Outline platelets.
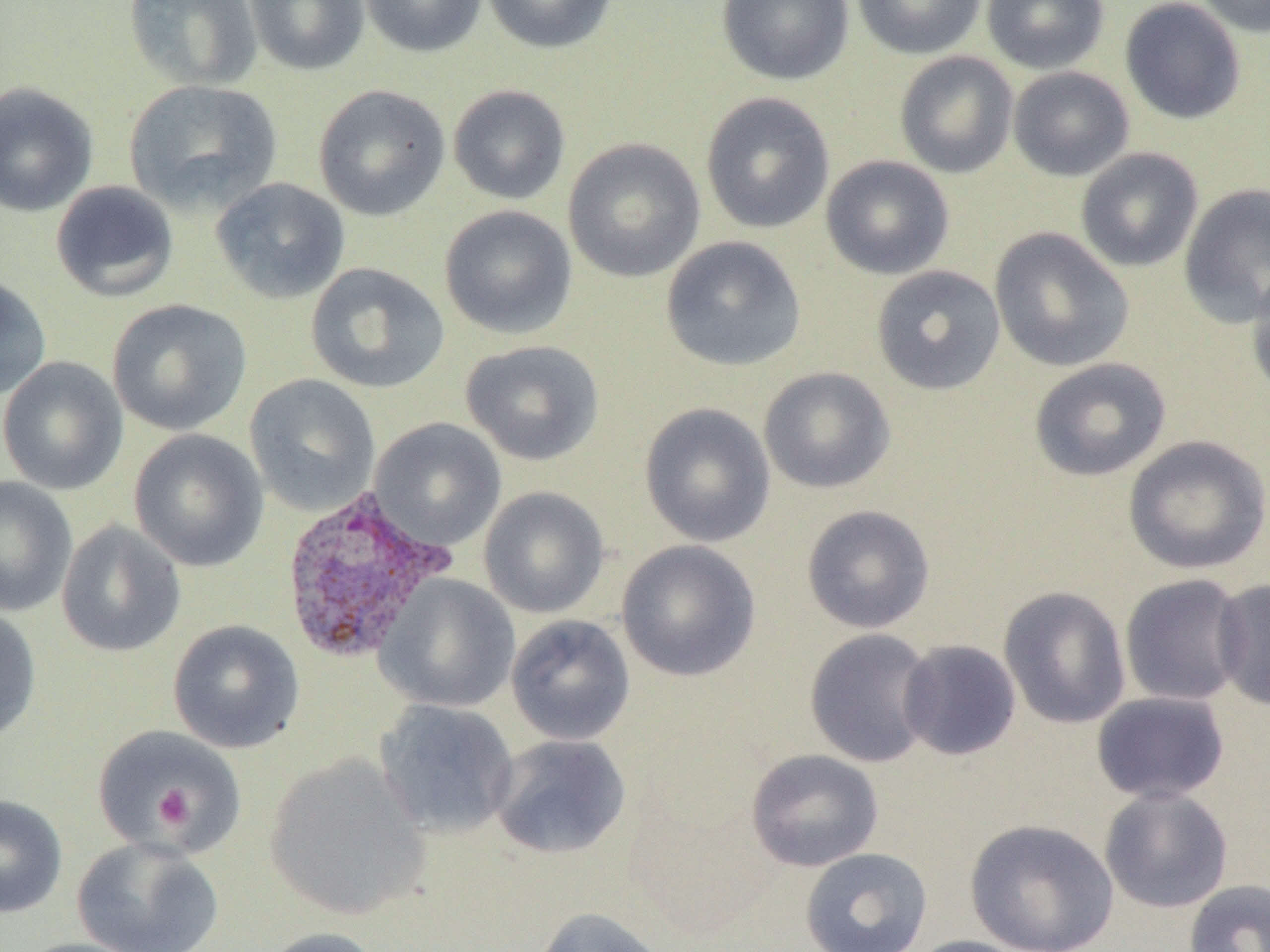
Approximate bounding boxes as named x1/y1/x2/y2 corners in pixels.
Platelets (subset): (x1=152, y1=785, x2=192, y2=829).

{
  "slide_level_diagnosis": "Plasmodium vivax",
  "field_of_view": "single",
  "uninfected_red_blood_cell_locations_subset": "approximate bounding boxes as named x1/y1/x2/y2 corners in pixels: (x1=123, y1=0, x2=263, y2=91), (x1=243, y1=0, x2=370, y2=76), (x1=358, y1=0, x2=488, y2=58), (x1=481, y1=0, x2=619, y2=55), (x1=716, y1=0, x2=853, y2=86), (x1=851, y1=0, x2=987, y2=60), (x1=981, y1=0, x2=1109, y2=74), (x1=1119, y1=0, x2=1247, y2=125), (x1=1193, y1=0, x2=1270, y2=37), (x1=894, y1=50, x2=1019, y2=179), (x1=1008, y1=66, x2=1134, y2=181), (x1=123, y1=79, x2=283, y2=217), (x1=0, y1=82, x2=98, y2=217), (x1=312, y1=84, x2=450, y2=221), (x1=447, y1=84, x2=571, y2=205), (x1=700, y1=91, x2=834, y2=234), (x1=562, y1=137, x2=706, y2=283), (x1=1075, y1=147, x2=1204, y2=272), (x1=820, y1=155, x2=955, y2=280), (x1=210, y1=177, x2=350, y2=303), (x1=50, y1=180, x2=179, y2=303), (x1=1179, y1=183, x2=1270, y2=327), (x1=439, y1=205, x2=578, y2=340), (x1=989, y1=227, x2=1134, y2=372), (x1=661, y1=236, x2=807, y2=372), (x1=305, y1=262, x2=450, y2=394), (x1=871, y1=265, x2=1006, y2=395), (x1=1246, y1=265, x2=1270, y2=406), (x1=0, y1=272, x2=52, y2=401), (x1=107, y1=298, x2=252, y2=436), (x1=460, y1=339, x2=604, y2=466), (x1=0, y1=355, x2=128, y2=496), (x1=1029, y1=357, x2=1172, y2=482), (x1=758, y1=367, x2=896, y2=494), (x1=243, y1=374, x2=381, y2=516), (x1=639, y1=402, x2=776, y2=548), (x1=369, y1=418, x2=506, y2=551), (x1=128, y1=429, x2=269, y2=572), (x1=1123, y1=435, x2=1270, y2=575), (x1=0, y1=476, x2=78, y2=616), (x1=478, y1=486, x2=610, y2=619), (x1=801, y1=504, x2=935, y2=634), (x1=56, y1=519, x2=186, y2=658), (x1=616, y1=540, x2=762, y2=682), (x1=1119, y1=573, x2=1249, y2=707), (x1=375, y1=574, x2=520, y2=713), (x1=1212, y1=578, x2=1270, y2=711), (x1=998, y1=586, x2=1131, y2=730), (x1=0, y1=604, x2=42, y2=745), (x1=505, y1=614, x2=636, y2=746), (x1=167, y1=619, x2=305, y2=754), (x1=804, y1=628, x2=937, y2=768), (x1=897, y1=639, x2=1021, y2=760), (x1=1091, y1=692, x2=1230, y2=804), (x1=373, y1=699, x2=519, y2=839), (x1=489, y1=734, x2=632, y2=860), (x1=745, y1=749, x2=884, y2=872), (x1=264, y1=752, x2=431, y2=921), (x1=1099, y1=787, x2=1234, y2=913), (x1=0, y1=793, x2=68, y2=918), (x1=965, y1=818, x2=1119, y2=952), (x1=71, y1=836, x2=224, y2=952), (x1=800, y1=847, x2=933, y2=952), (x1=1183, y1=879, x2=1270, y2=952), (x1=532, y1=906, x2=671, y2=952), (x1=256, y1=926, x2=387, y2=952), (x1=903, y1=935, x2=1039, y2=952), (x1=13, y1=937, x2=154, y2=952)",
  "image_size": "1270×952 pixels",
  "magnification": "1000x",
  "plasmodium_vivax_infected_red_blood_cell_locations": "approximate bounding boxes as named x1/y1/x2/y2 corners in pixels: (x1=278, y1=487, x2=457, y2=666)",
  "preparation": "thin blood smear",
  "modality": "light microscopy"
}